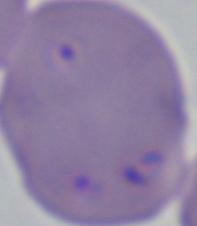

{
  "identification": "Babesia",
  "modality": "photomicrograph",
  "magnification": "1000x"
}